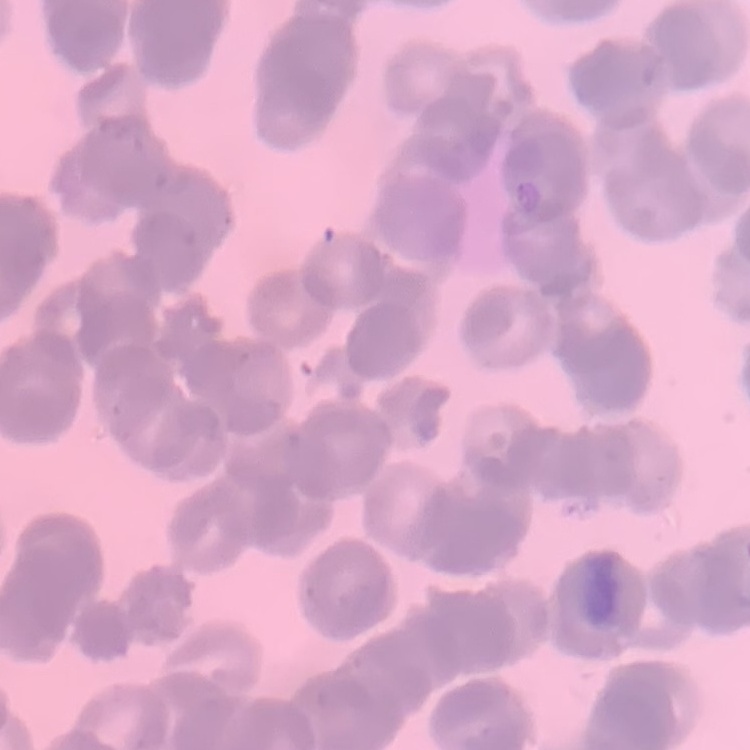

erythrocyte morphology = rouleaux formation
stain = Field's or Giemsa
image type = one tile cut from a larger photomicrograph
preparation = thin blood film